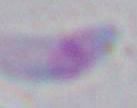

1000x magnification. Toxoplasma gondii is seen. Photomicrograph.